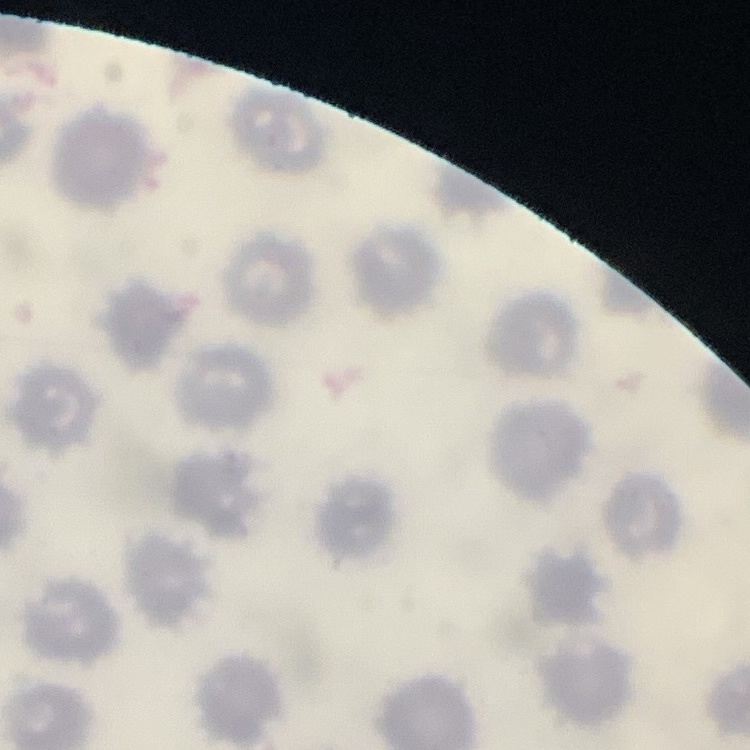
Summary:
  - Erythrocyte morphology: no rouleaux formation
  - Stain: Field's or Giemsa
  - Image type: one tile cut from a larger photomicrograph
  - Preparation: thin peripheral smear